Give the extent of all uninfected red blood cells.
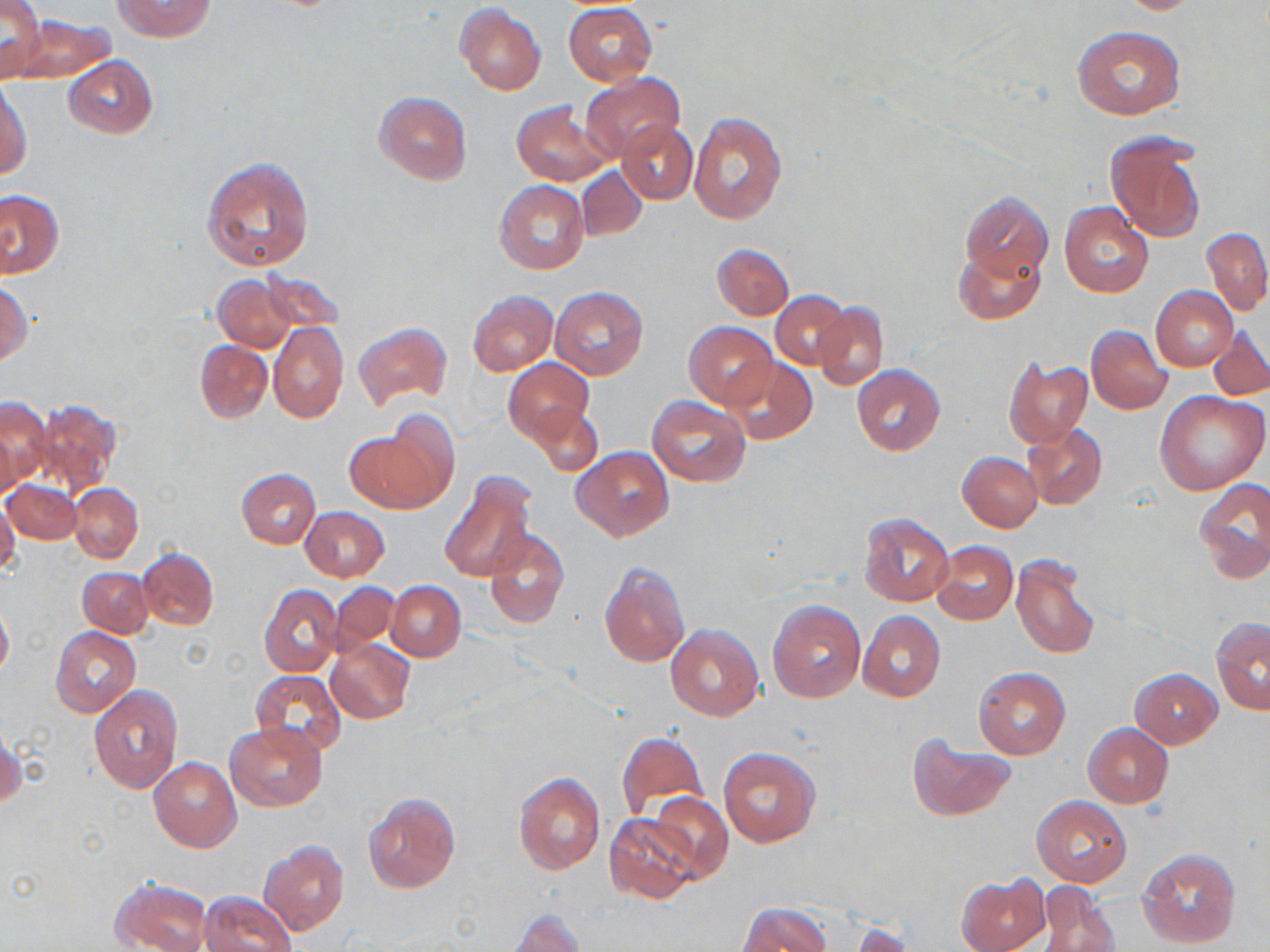
Approximate bounding boxes as [x1, y1, x2, y2] in pixels.
Uninfected red blood cells: [0, 0, 43, 81], [113, 0, 216, 43], [1114, 0, 1209, 15], [563, 2, 657, 85], [455, 4, 547, 96], [13, 14, 116, 84], [1074, 26, 1184, 119], [63, 56, 157, 137], [579, 72, 685, 162], [0, 79, 33, 182], [373, 90, 472, 185], [512, 101, 614, 184], [687, 110, 787, 224], [617, 119, 696, 202], [1107, 135, 1206, 243], [201, 156, 316, 272], [577, 167, 646, 241], [495, 180, 589, 275], [1, 189, 63, 278], [960, 191, 1053, 284], [1059, 201, 1154, 297], [1203, 227, 1270, 315], [712, 244, 794, 319], [952, 244, 1044, 325], [255, 268, 342, 334], [214, 275, 299, 352], [1, 283, 32, 365], [1151, 286, 1238, 372], [551, 287, 647, 380], [468, 290, 557, 374], [772, 291, 853, 370], [814, 303, 889, 389], [353, 321, 452, 410], [685, 321, 776, 409], [270, 323, 349, 423], [1087, 325, 1172, 414], [1208, 327, 1270, 400], [195, 341, 272, 422], [1004, 356, 1094, 449], [504, 357, 594, 444], [727, 357, 816, 444], [853, 365, 946, 454], [1156, 390, 1269, 494], [646, 395, 751, 486], [0, 398, 48, 496], [30, 398, 120, 495], [529, 401, 603, 475], [346, 425, 454, 513], [1023, 425, 1108, 509], [572, 447, 674, 541], [958, 451, 1043, 531], [236, 468, 321, 548], [440, 472, 537, 582], [1194, 478, 1270, 584], [5, 479, 81, 543], [69, 482, 144, 563], [0, 499, 20, 576], [301, 507, 389, 581], [858, 512, 954, 607], [482, 529, 570, 628], [932, 541, 1018, 625], [137, 548, 218, 631], [1011, 553, 1101, 659], [600, 562, 690, 668], [78, 567, 153, 636], [386, 581, 465, 661], [330, 583, 400, 652], [259, 584, 343, 677], [768, 600, 867, 704], [0, 601, 13, 680], [858, 611, 944, 701], [1211, 617, 1269, 715], [665, 624, 764, 720], [51, 626, 142, 717], [325, 638, 414, 723], [973, 667, 1071, 759], [1131, 669, 1223, 749], [252, 670, 346, 757], [89, 684, 182, 792], [226, 721, 327, 811], [1083, 723, 1174, 807], [0, 728, 24, 810], [615, 732, 708, 820], [909, 737, 1015, 820], [719, 748, 821, 848], [149, 757, 242, 851], [514, 772, 605, 873], [648, 792, 733, 880], [364, 793, 460, 892], [1032, 796, 1132, 887], [605, 812, 699, 904], [260, 840, 349, 935], [1137, 846, 1240, 949], [957, 874, 1049, 952], [111, 877, 213, 952], [1034, 883, 1122, 952], [199, 891, 297, 952], [739, 903, 832, 952], [507, 910, 585, 952], [844, 923, 916, 951].

Summary:
  - Slide-level diagnosis: negative for blood parasites
  - Modality: light microscopy
  - Magnification: 1000x
  - Image size: 1270×952 pixels
  - Field of view: single
  - Preparation: thin blood film
  - Stain: May-Grünwald-Giemsa